Point out Plasmodium parasites and leukocytes.
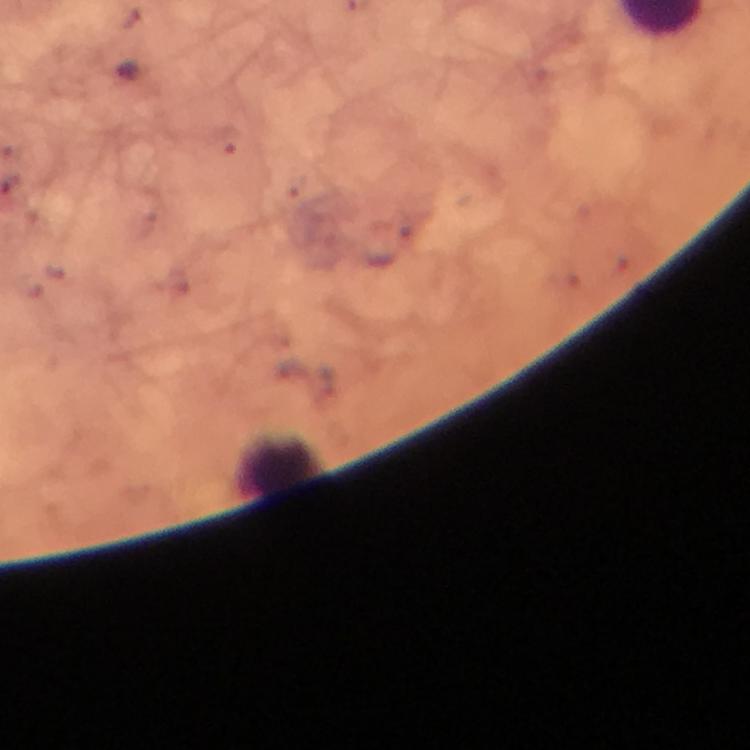

No Plasmodium parasites seen.
Approximate centers as [x, y] in pixels.
Leukocytes: [278, 465].

image_size: 750×750 pixels
preparation: thick blood film
cropped_from: one field of view
magnification: 100x
immersion_oil: applied
context: from a diagnostic examination for malaria
stain: Giemsa
capture: smartphone mounted on the microscope